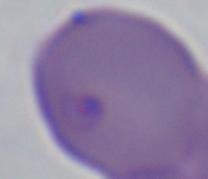
magnification = 1000x
identification = Babesia
modality = photomicrograph